Identify the blood parasite species.
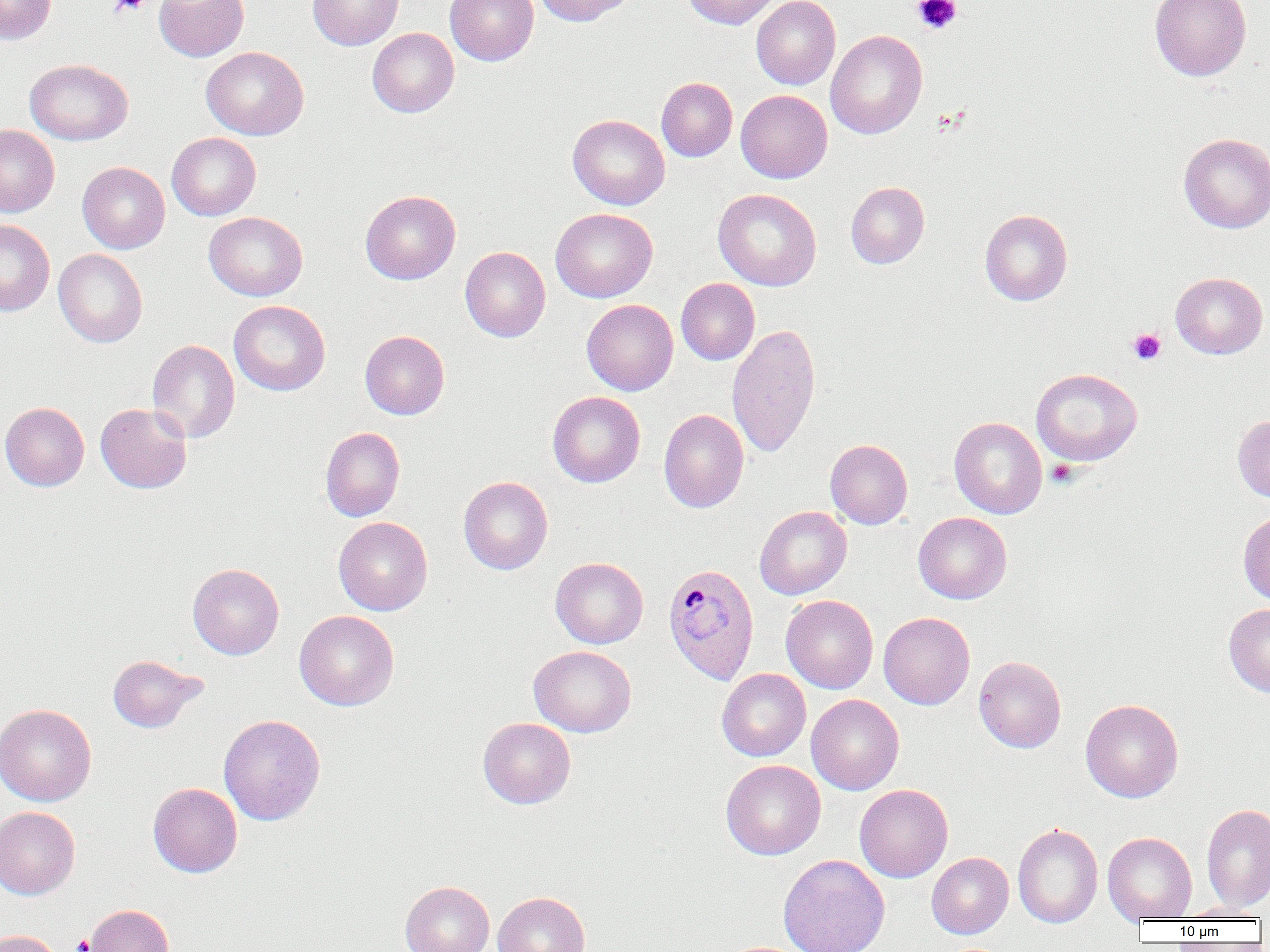

Plasmodium ovale.

Summary:
  - Coordinate format: approximate bounding boxes as (x1,y1)-(x2,y2) corner pairs in pixels
  - Plasmodium ovale-infected red blood cell locations: (663,563)-(759,685)
  - Uninfected red blood cell locations: (0,0)-(56,44), (154,0)-(249,61), (308,0)-(403,50), (444,0)-(539,65), (534,0)-(636,26), (682,0)-(781,29), (751,0)-(840,90), (1149,0)-(1252,81), (367,28)-(459,117), (825,30)-(927,139), (201,46)-(309,140), (25,59)-(133,145), (656,77)-(737,162), (736,89)-(833,183), (567,114)-(670,210), (0,125)-(59,217), (1179,132)-(1270,233), (167,133)-(261,220), (77,162)-(170,253), (846,182)-(930,269), (712,188)-(822,291), (360,190)-(460,284), (550,208)-(657,302), (980,209)-(1073,306), (203,212)-(307,301), (0,219)-(54,317), (460,247)-(550,342), (53,249)-(148,347), (1170,272)-(1268,359), (676,278)-(760,365), (582,299)-(678,395), (229,300)-(330,396), (726,324)-(821,458), (360,330)-(450,419), (146,339)-(240,443), (1030,368)-(1142,466), (547,391)-(645,488), (0,402)-(89,491), (95,403)-(192,494), (658,409)-(749,512), (1233,414)-(1270,503), (949,416)-(1047,519), (320,427)-(405,521), (825,439)-(913,529), (458,476)-(553,575), (754,506)-(852,599), (1238,511)-(1270,606), (913,512)-(1012,604), (333,516)-(433,616), (550,557)-(648,649), (187,563)-(284,659), (781,595)-(878,693), (1224,603)-(1270,697), (294,610)-(399,710), (878,612)-(975,710), (529,645)-(636,737), (107,654)-(205,733), (973,655)-(1067,753), (716,668)-(811,761), (806,694)-(904,795), (1081,699)-(1183,802), (0,703)-(97,806), (218,714)-(326,826), (477,717)-(576,809), (720,759)-(825,860), (147,782)-(243,877), (854,784)-(953,882), (1201,803)-(1270,912), (0,806)-(80,900), (1012,822)-(1103,928), (1103,832)-(1197,922), (926,852)-(1013,938), (778,854)-(890,952), (400,881)-(495,952), (493,891)-(591,952), (84,904)-(174,952), (1175,904)-(1267,921), (0,930)-(62,952)
  - Platelet locations: (108,0)-(150,17), (912,0)-(962,34), (1127,328)-(1166,365), (1046,459)-(1078,488), (71,935)-(93,952)
  - Image size: 1270×952 pixels
  - Field of view: single
  - Magnification: 1000x
  - Preparation: thin blood smear
  - Modality: light microscopy